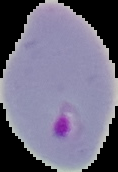
image_type: segmented cell region with the area outside set to black
preparation: thin blood smear
image_size: 118×172 pixels
malaria_status: parasitized